Name the cell type shown.
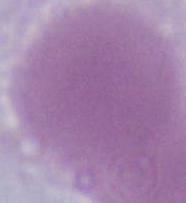
This is an erythrocyte.

modality = micrograph
magnification = 1000x